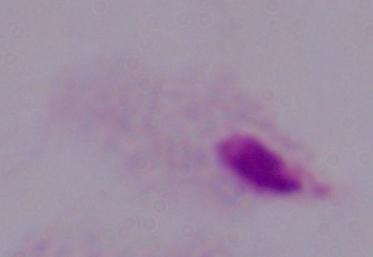

Summary:
  - Modality: photomicrograph
  - Magnification: 1000x
  - Identification: trichomonad